Assess this cell for malaria.
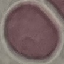

Uninfected.

preparation = thin blood film
image type = cell patch, automatically extracted from a larger field of view and resized to 64 × 64 pixels
stain = Giemsa
capture = smartphone camera at the microscope eyepiece